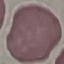 Malaria status: uninfected. Giemsa-stained preparation. Cell patch, automatically extracted from a larger field of view and resized to 64 × 64 pixels. Acquired by smartphone through the microscope eyepiece. Thin smear of blood.